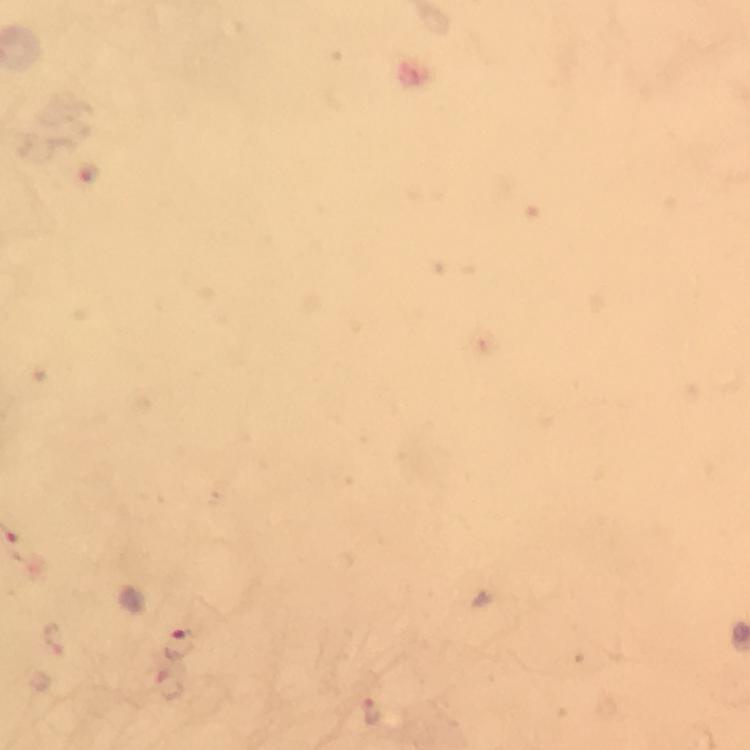
cropped from = a single field of view
stain = Giemsa
capture = smartphone mounted on the microscope
magnification = 100x
preparation = thick blood smear
context = from a diagnostic examination for malaria
immersion oil = used
Plasmodium parasite locations = approximate centers as (x, y) in pixels: (88, 173), (180, 643), (373, 712)
image size = 750×750 pixels